Give the position of every Plasmodium parasite visible.
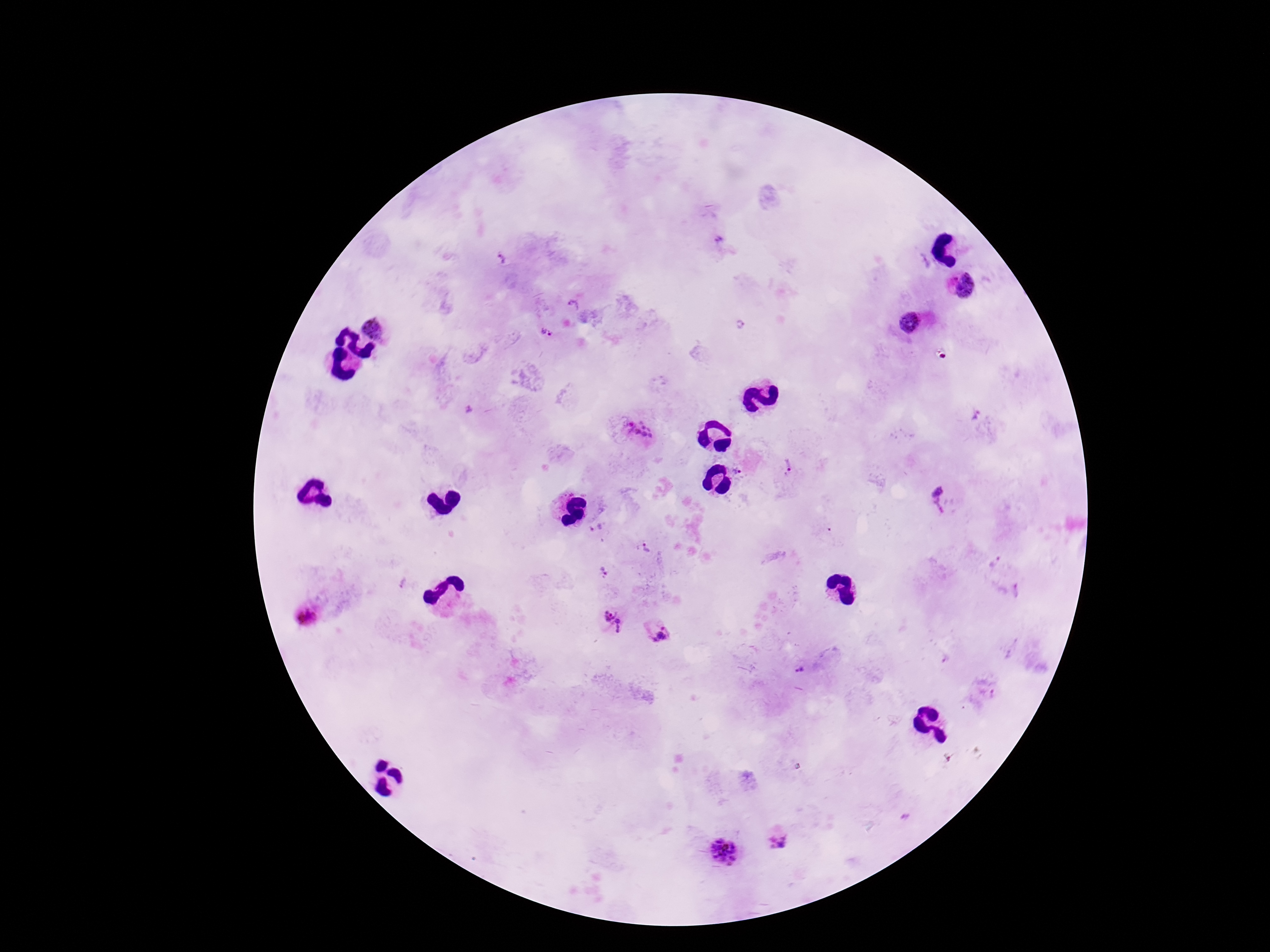

Approximate centers as {x, y} in pixels.
Plasmodium parasites: {719, 239}, {502, 259}, {968, 285}, {573, 306}, {910, 321}, {376, 326}, {547, 332}, {469, 410}, {975, 416}, {642, 428}, {788, 465}, {737, 471}, {937, 489}, {940, 507}, {597, 530}, {646, 548}, {994, 562}, {602, 570}, {404, 582}, {307, 616}, {613, 621}, {660, 632}, {800, 670}, {778, 842}, {725, 852}.

stain = Giemsa
capture = smartphone camera through the microscope eyepiece
image size = 1270×952 pixels
patient malaria status = infected
field of view = one from this slide
magnification = 100x
preparation = thick blood film